Report the malaria status of this cell.
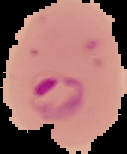

Parasitized.

{
  "preparation": "thin blood smear",
  "image_type": "segmented cell region with the area outside set to black",
  "image_size": "127×154 pixels"
}